State which parasite is depicted.
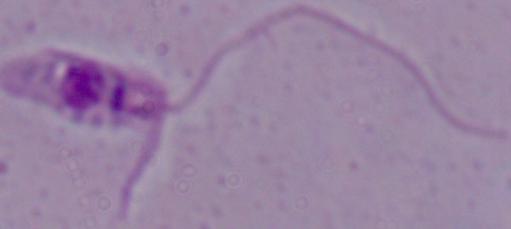

This is Leishmania.

Summary:
  - Modality: micrograph
  - Magnification: 1000x